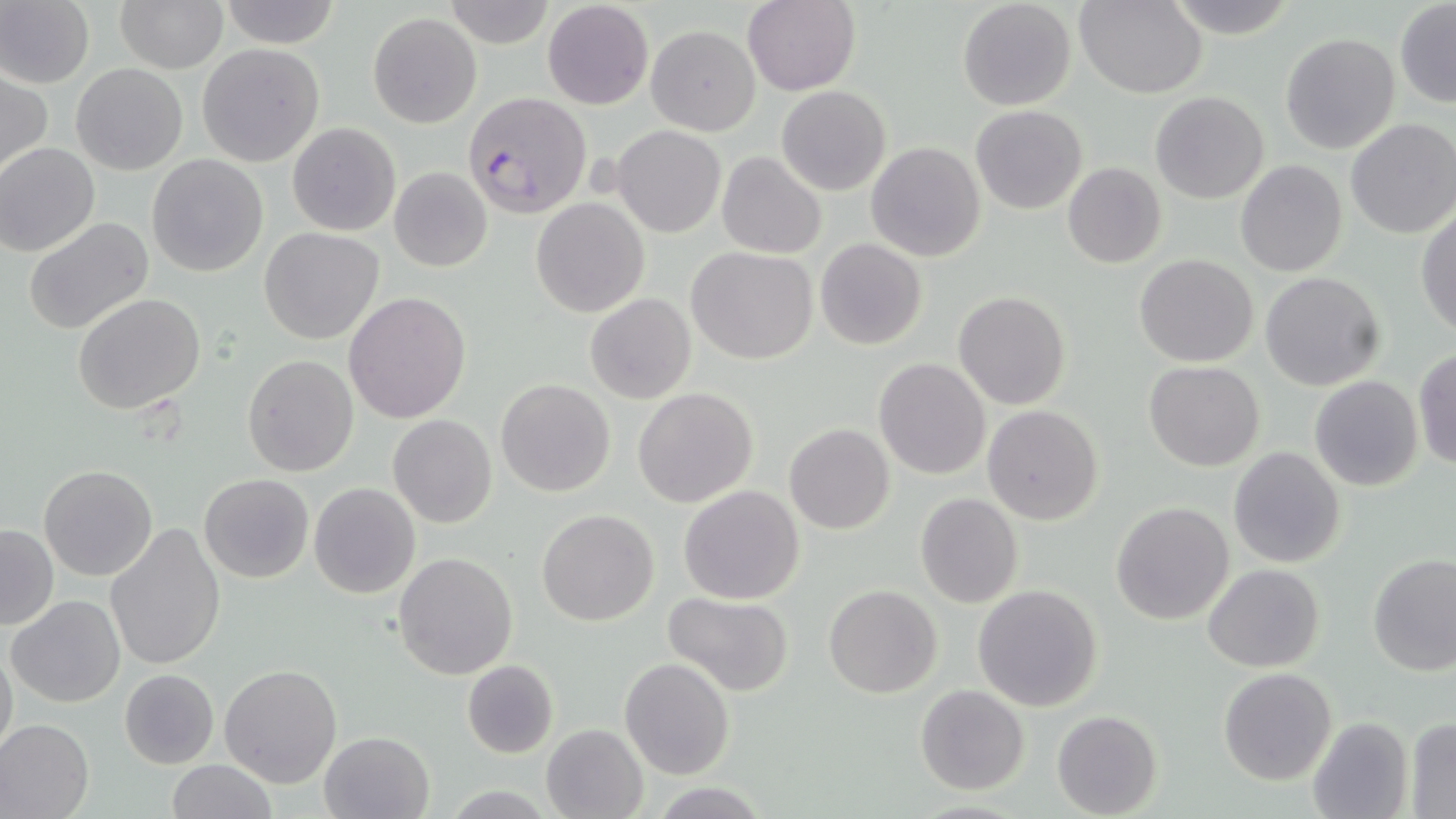
Summary:
  - Coordinate format: approximate bounding boxes as [x1, y1, x2, y2] in pixels
  - Uninfected red blood cell locations: [0, 0, 94, 88], [114, 0, 227, 72], [218, 0, 342, 48], [742, 0, 859, 94], [957, 0, 1076, 111], [1077, 0, 1206, 97], [446, 1, 553, 48], [1162, 1, 1298, 37], [542, 2, 653, 110], [1395, 2, 1456, 107], [368, 11, 481, 129], [647, 25, 760, 135], [1280, 32, 1399, 154], [197, 43, 324, 166], [70, 63, 187, 175], [1, 71, 51, 178], [777, 86, 891, 196], [1150, 91, 1269, 204], [971, 106, 1087, 214], [1345, 118, 1456, 239], [287, 122, 400, 236], [612, 125, 725, 238], [866, 141, 985, 262], [1, 143, 100, 256], [717, 152, 825, 258], [146, 154, 268, 277], [1235, 160, 1348, 277], [1062, 162, 1166, 267], [389, 166, 492, 273], [532, 198, 648, 317], [1416, 208, 1456, 340], [24, 217, 153, 335], [260, 228, 385, 345], [814, 239, 927, 351], [687, 247, 818, 365], [1135, 254, 1257, 367], [1259, 272, 1385, 390], [954, 291, 1070, 410], [73, 293, 206, 414], [343, 293, 471, 424], [585, 293, 696, 404], [1413, 346, 1456, 471], [243, 355, 358, 476], [873, 357, 992, 478], [1144, 360, 1265, 472], [1310, 375, 1424, 491], [495, 378, 615, 496], [632, 387, 758, 509], [982, 405, 1104, 526], [389, 414, 498, 529], [784, 424, 895, 534], [1229, 446, 1346, 568], [40, 466, 159, 582], [199, 474, 313, 584], [310, 482, 421, 599], [679, 484, 804, 604], [915, 493, 1024, 609], [1111, 501, 1234, 623], [537, 508, 659, 626], [2, 523, 58, 631], [106, 524, 227, 671], [393, 551, 520, 680], [1366, 554, 1456, 676], [1204, 563, 1325, 673], [972, 584, 1104, 712], [824, 585, 943, 698], [661, 590, 796, 696], [8, 595, 126, 708], [0, 641, 18, 759], [620, 657, 735, 781], [461, 659, 559, 758], [220, 663, 341, 788], [1220, 667, 1336, 786], [118, 668, 218, 767], [916, 685, 1029, 795], [1051, 711, 1162, 818], [1306, 716, 1412, 818], [0, 717, 94, 819], [1404, 718, 1456, 815], [541, 723, 649, 818], [319, 731, 436, 819], [166, 759, 275, 818], [651, 782, 770, 818]
  - Plasmodium falciparum-infected red blood cell locations: [464, 93, 590, 218]
  - Slide-level diagnosis: Plasmodium falciparum
  - Stain: May-Grünwald-Giemsa
  - Modality: optical microscopy
  - Field of view: one of a larger specimen
  - Magnification: 1000x
  - Preparation: thin blood film
  - Image size: 1456×819 pixels